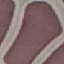
Summary:
  - Malaria status: uninfected
  - Capture: smartphone camera at the microscope eyepiece
  - Image type: automatically extracted cell patch, resized to 64 × 64 pixels
  - Stain: Giemsa
  - Preparation: thin smear